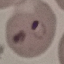

malaria status = parasitized
preparation = thin blood film
capture = smartphone camera at the microscope eyepiece
stain = Giemsa
image type = cell patch, automatically extracted from a larger field of view and resized to 64 × 64 pixels